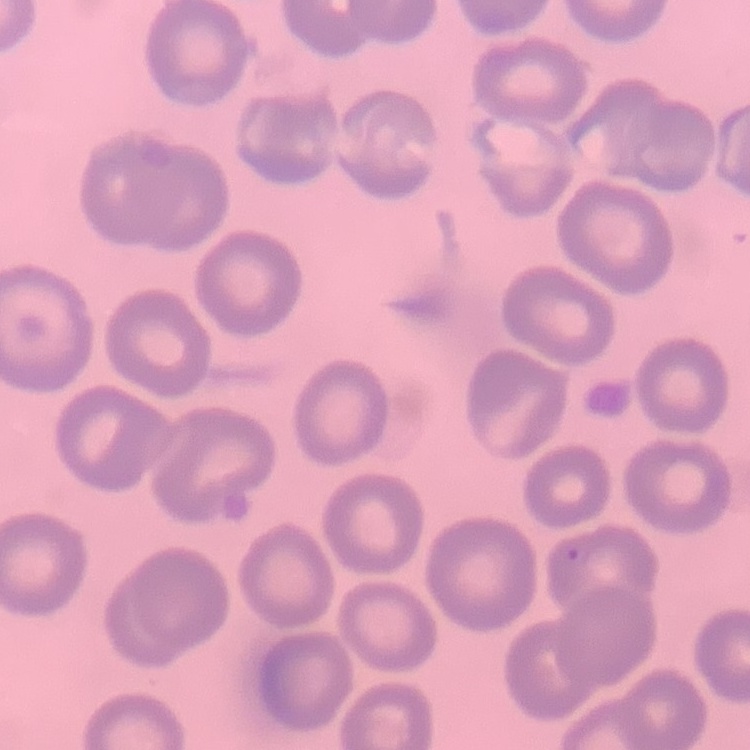

The erythrocytes show no rouleaux formation. Thin blood smear. One tile cut from a larger photomicrograph. Field's or Giemsa stain.